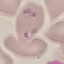 Result: no malaria parasites detected. Thin smear of blood. Acquired by smartphone through the microscope eyepiece. Automatically extracted cell patch, resized to 64 × 64 pixels. Giemsa stain.